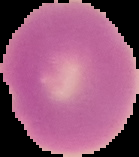
Summary:
  - Preparation: thin blood film
  - Image size: 139×157 pixels
  - Image type: segmented cell region with the area outside set to black
  - Malaria status: uninfected